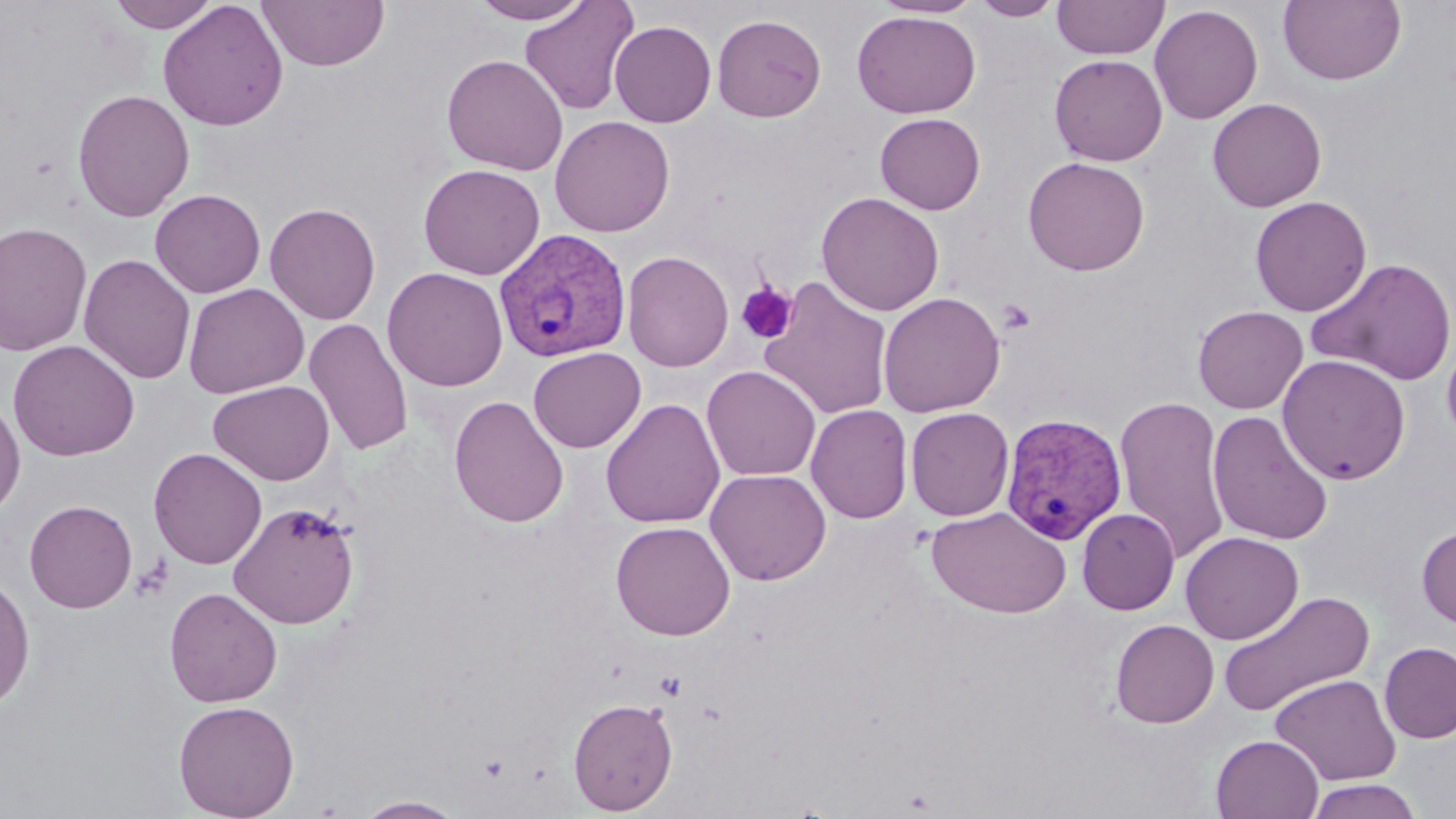

Summary:
  - Coordinate format: approximate bounding boxes as [x1, y1, x2, y2] in pixels
  - Uninfected red blood cell locations: [107, 0, 221, 33], [157, 0, 289, 132], [256, 0, 389, 72], [469, 0, 593, 24], [872, 0, 984, 19], [971, 0, 1064, 20], [1052, 0, 1169, 60], [1278, 0, 1406, 86], [520, 1, 639, 116], [1149, 4, 1263, 125], [852, 10, 981, 118], [712, 14, 827, 122], [609, 21, 716, 127], [441, 54, 568, 175], [1049, 54, 1168, 166], [72, 89, 195, 222], [1207, 97, 1327, 212], [875, 112, 986, 215], [550, 115, 675, 237], [1023, 156, 1150, 275], [418, 163, 545, 280], [150, 188, 265, 298], [816, 191, 944, 316], [1250, 195, 1372, 317], [265, 202, 381, 325], [0, 222, 93, 356], [622, 250, 734, 372], [79, 253, 196, 384], [1306, 257, 1456, 386], [382, 267, 508, 391], [759, 277, 894, 421], [183, 283, 309, 399], [877, 291, 1006, 417], [1193, 305, 1308, 414], [304, 318, 414, 457], [1441, 322, 1456, 448], [7, 339, 140, 462], [528, 347, 646, 452], [1277, 354, 1411, 485], [702, 365, 821, 481], [208, 380, 334, 485], [0, 395, 25, 517], [448, 395, 569, 528], [1114, 396, 1231, 566], [600, 398, 726, 529], [806, 404, 913, 524], [905, 407, 1014, 521], [1207, 410, 1334, 546], [149, 447, 267, 569], [704, 468, 831, 586], [24, 499, 138, 613], [228, 501, 361, 629], [926, 506, 1072, 619], [1077, 508, 1180, 615], [610, 520, 735, 640], [1417, 524, 1456, 628], [1180, 531, 1303, 644], [0, 576, 35, 712], [164, 587, 282, 707], [1216, 590, 1376, 718], [1110, 619, 1219, 728], [1378, 641, 1456, 744], [1270, 674, 1400, 785], [568, 697, 678, 815], [173, 699, 300, 819], [1211, 734, 1323, 818], [1305, 779, 1423, 819], [355, 795, 467, 818]
  - Platelet locations: [735, 282, 798, 344], [996, 298, 1038, 334]
  - Plasmodium vivax-infected red blood cell locations: [493, 227, 631, 363], [1000, 412, 1128, 546]
  - Slide-level diagnosis: Plasmodium vivax
  - Modality: optical microscopy
  - Preparation: thin blood film
  - Magnification: 1000x
  - Field of view: one of a larger specimen
  - Stain: May-Grünwald-Giemsa
  - Image size: 1456×819 pixels